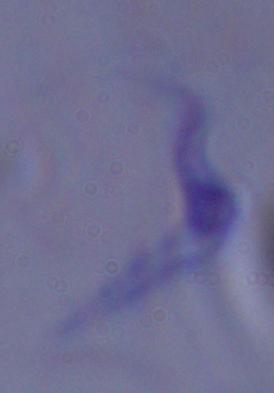

{
  "modality": "photomicrograph",
  "magnification": "1000x",
  "identification": "trypanosome"
}